Classify this cell by malaria status.
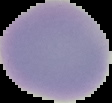
It is uninfected.

Summary:
  - Image type: segmented cell region with the area outside set to black
  - Preparation: thin blood film
  - Image size: 112×103 pixels